Point out each Plasmodium parasite.
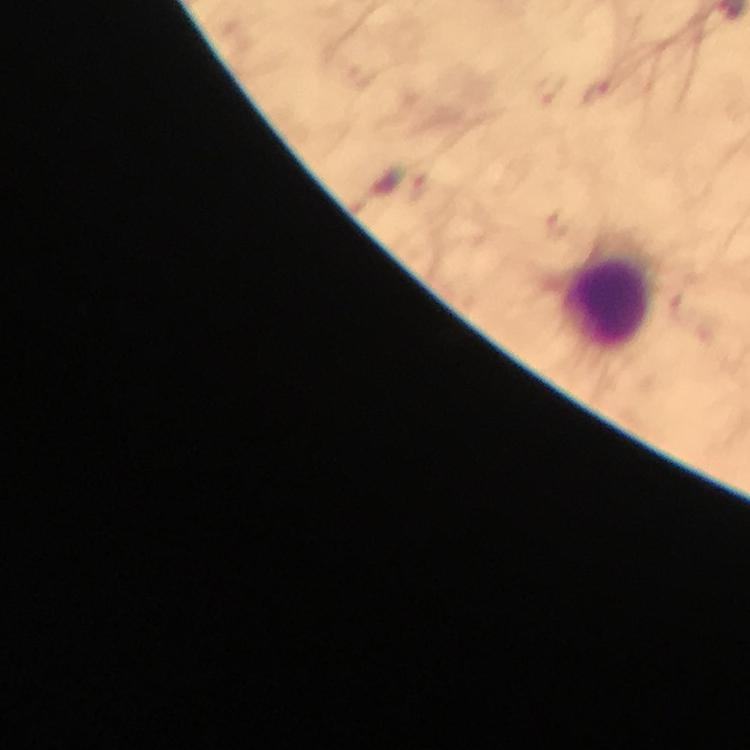

Approximate centers as [x, y] in pixels.
Plasmodium parasites: [600, 94].

Leukocyte locations: [608, 301]. From a diagnostic examination for malaria. Image is 750×750 pixels. Immersion oil was used. Thick smear. Giemsa-stained preparation. 100x magnification. Smartphone photograph taken through a microscope. A crop from one field of view.